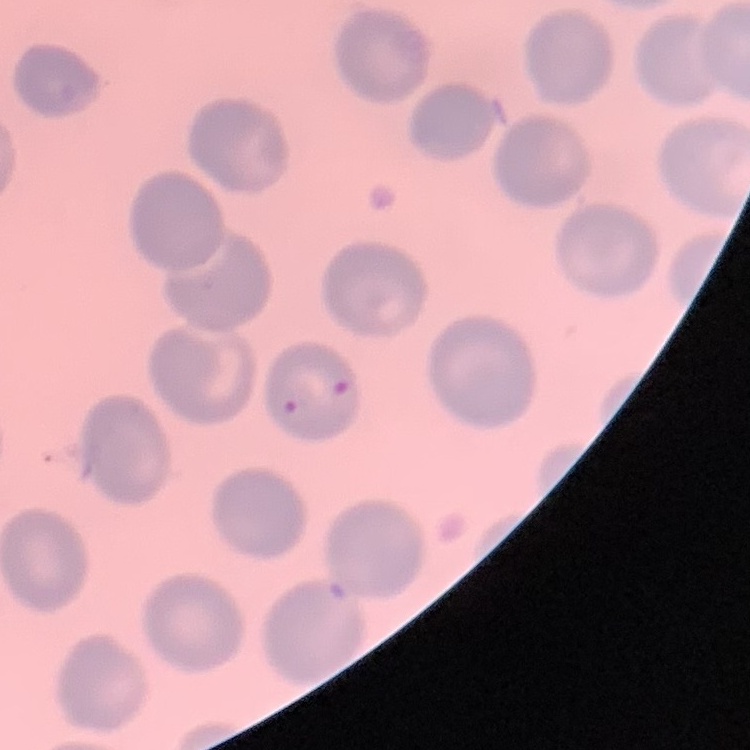

erythrocyte morphology = no rouleaux formation
stain = Field's or Giemsa
image type = square crop of a larger photomicrograph
preparation = thin blood smear